Locate malaria parasites and leukocytes.
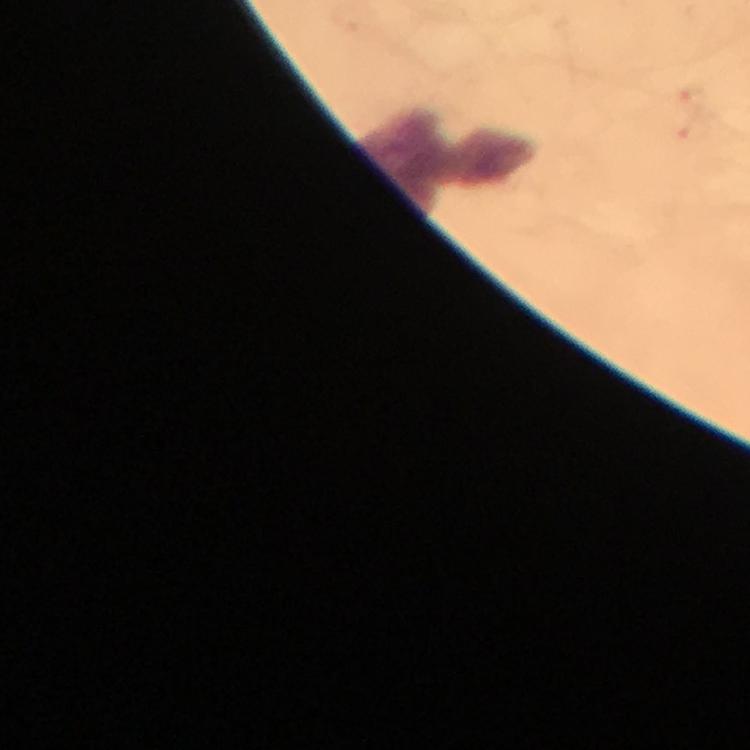
No malaria parasites detected.
Approximate centers as [x, y] in pixels.
Leukocytes: [446, 161].

Summary:
  - Stain: Giemsa
  - Capture: smartphone photograph through a microscope
  - Immersion oil: used
  - Image size: 750×750 pixels
  - Preparation: thick blood smear
  - Context: from a malaria diagnostic workup
  - Cropped from: a single field of view
  - Magnification: 100x